Outline each Plasmodium ovale-infected red blood cell.
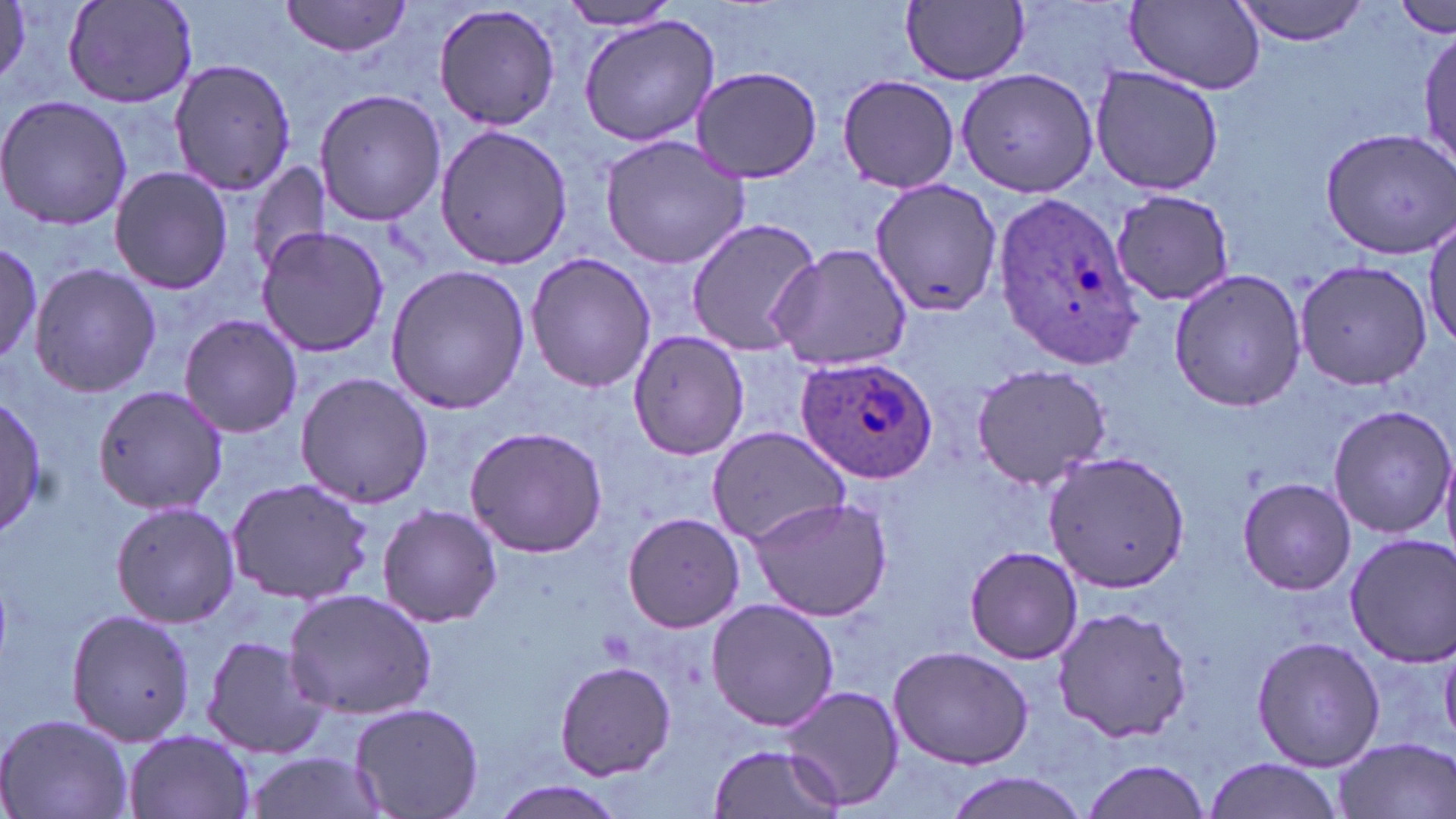
Approximate bounding boxes as (x1,y1)-(x2,y2) corner pairs in pixels.
Plasmodium ovale-infected red blood cells: (991,192)-(1147,370), (794,354)-(937,484).

Summary:
  - Uninfected red blood cell locations: (281,0)-(412,59), (1125,0)-(1265,92), (1230,0)-(1370,46), (64,1)-(198,108), (555,1)-(683,33), (902,1)-(1028,86), (1394,2)-(1454,37), (431,3)-(562,133), (578,16)-(718,148), (1416,23)-(1454,171), (167,58)-(297,198), (690,64)-(823,184), (1088,64)-(1224,196), (956,66)-(1102,198), (836,73)-(959,194), (315,88)-(446,226), (0,94)-(132,232), (433,123)-(571,272), (1321,125)-(1456,257), (598,133)-(752,271), (248,161)-(330,275), (109,166)-(232,295), (866,176)-(1001,319), (1109,188)-(1238,308), (1426,212)-(1456,351), (684,216)-(824,356), (255,227)-(391,359), (0,243)-(60,381), (769,243)-(916,374), (524,253)-(657,392), (1294,258)-(1433,392), (27,263)-(161,397), (384,265)-(531,415), (1168,270)-(1307,415), (179,315)-(303,438), (629,331)-(749,459), (970,362)-(1109,490), (294,372)-(435,509), (93,385)-(226,515), (1,394)-(51,535), (1325,405)-(1456,538), (462,423)-(610,558), (705,426)-(853,545), (1044,451)-(1191,592), (224,477)-(376,605), (1237,477)-(1354,595), (745,493)-(893,622), (110,499)-(240,629), (376,503)-(503,627), (621,512)-(744,634), (1341,532)-(1456,666), (963,544)-(1085,665), (281,589)-(438,721), (705,598)-(840,732), (1051,607)-(1191,742), (65,608)-(195,747), (199,633)-(332,759), (1250,635)-(1386,772), (886,645)-(1035,770), (554,659)-(677,782), (777,684)-(905,812), (345,703)-(485,818), (0,713)-(133,819), (122,730)-(257,819), (1332,735)-(1454,819), (708,741)-(844,818), (243,751)-(383,819), (1077,755)-(1213,819), (1201,757)-(1349,819), (940,772)-(1090,819), (490,781)-(627,819)
  - Slide-level diagnosis: Plasmodium ovale
  - Image size: 1456×819 pixels
  - Preparation: thin blood film
  - Stain: May-Grünwald-Giemsa
  - Field of view: single
  - Modality: optical microscopy
  - Magnification: 1000x